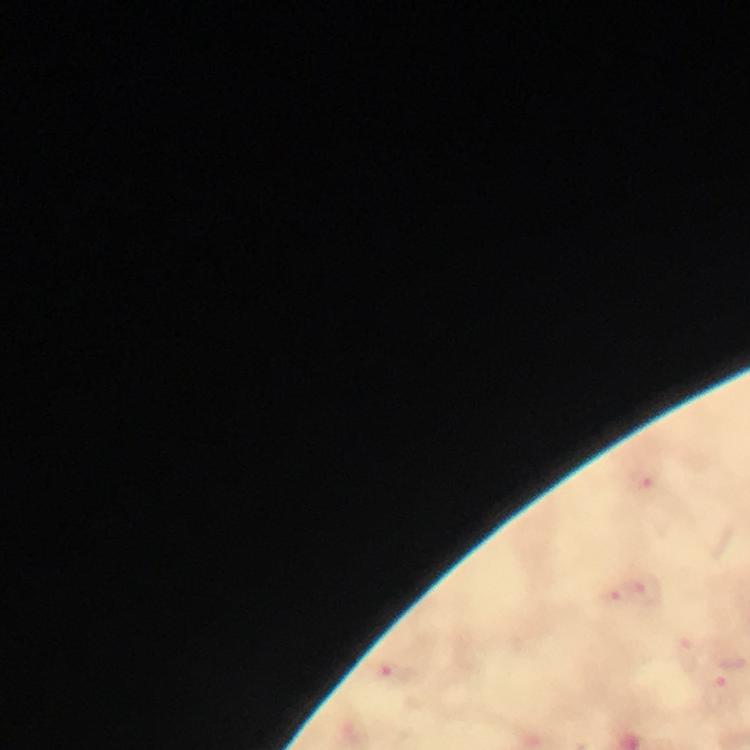

Approximate object centers, in pixels from the top-left corner.
Summary:
  - Malaria parasite locations: (x=646, y=478), (x=648, y=593), (x=396, y=674)
  - Image size: 750×750 pixels
  - Magnification: 100x
  - Capture: smartphone photograph through a microscope
  - Stain: Giemsa
  - Context: from a malaria diagnostic workup
  - Preparation: thick smear
  - Immersion oil: applied
  - Cropped from: one field of view